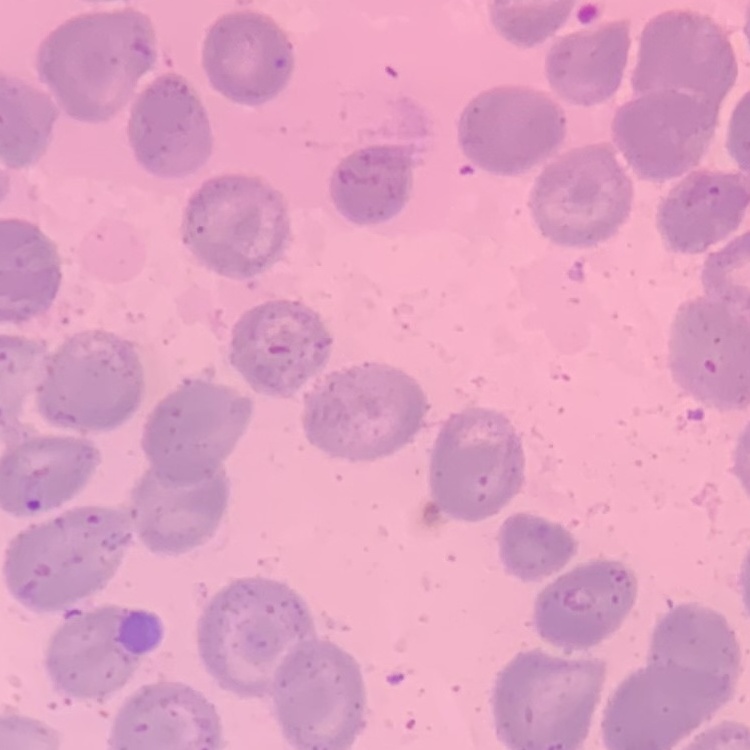
erythrocyte morphology = no rouleaux formation
preparation = thin blood film
image type = one tile cut from a larger photomicrograph
stain = Field's or Giemsa